Outline each Plasmodium ovale-infected red blood cell.
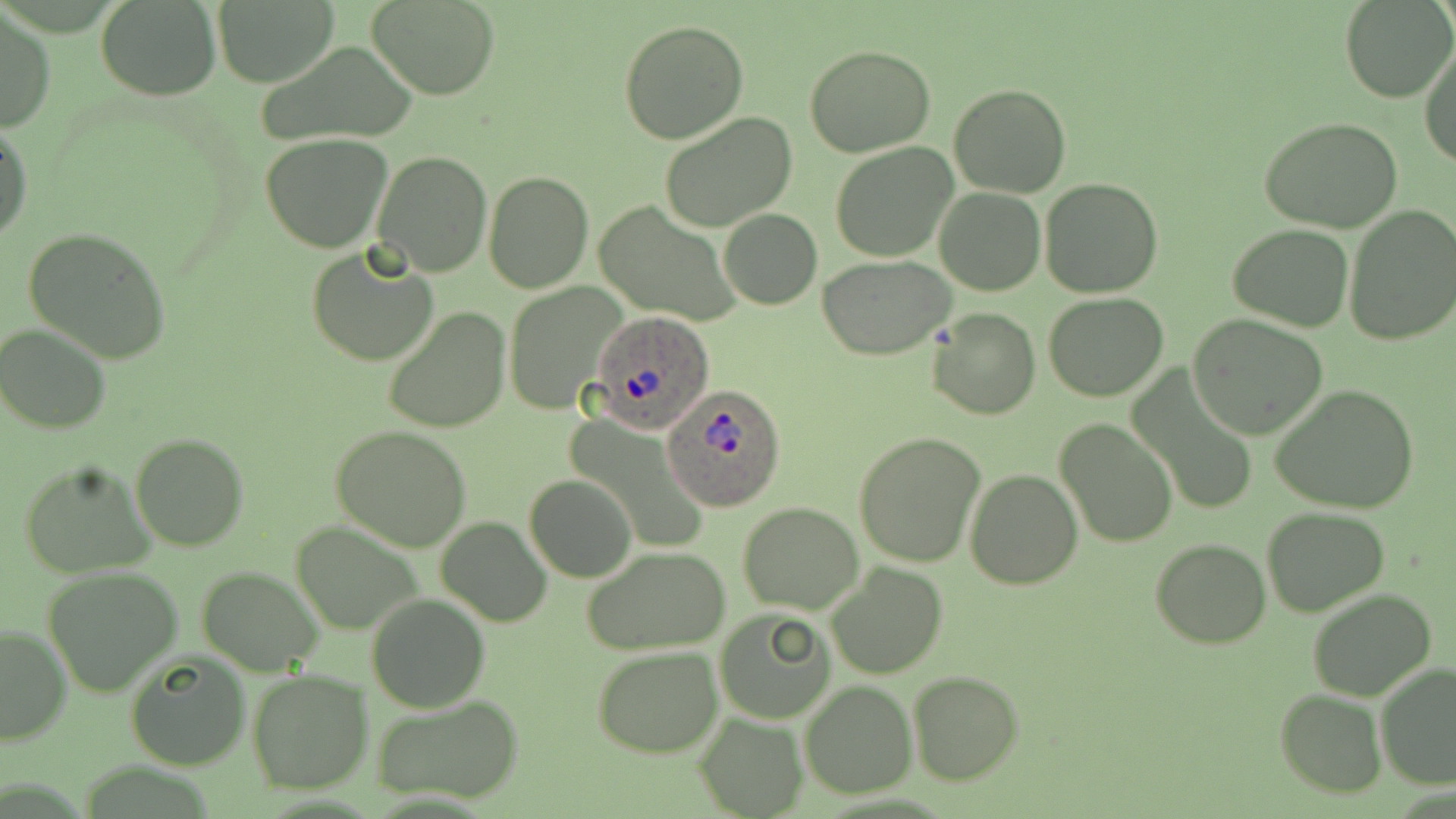

Approximate bounding boxes as (x1, y1, x2, y2) in pixels.
Plasmodium ovale-infected red blood cells: (587, 311, 719, 438), (667, 385, 788, 510).

Summary:
  - Uninfected red blood cell locations: (367, 0, 499, 99), (1340, 0, 1454, 103), (97, 1, 219, 100), (211, 2, 334, 83), (1, 8, 54, 134), (618, 19, 749, 144), (254, 39, 420, 150), (1419, 43, 1456, 167), (804, 44, 937, 157), (949, 84, 1072, 199), (659, 111, 798, 232), (1259, 116, 1404, 233), (0, 118, 33, 245), (261, 134, 394, 252), (831, 142, 960, 262), (370, 151, 493, 278), (482, 171, 595, 294), (1040, 177, 1163, 298), (934, 187, 1045, 296), (594, 199, 740, 326), (1343, 204, 1456, 344), (719, 210, 821, 310), (1228, 223, 1356, 331), (22, 227, 171, 364), (305, 245, 439, 369), (820, 255, 956, 359), (506, 283, 627, 415), (1044, 291, 1168, 401), (382, 306, 512, 433), (927, 307, 1040, 420), (1189, 313, 1329, 440), (1, 324, 113, 433), (1127, 366, 1261, 521), (1269, 384, 1420, 514), (1054, 418, 1179, 549), (330, 424, 476, 554), (855, 430, 985, 568), (130, 431, 249, 552), (17, 458, 155, 579), (964, 468, 1083, 589), (525, 474, 636, 583), (737, 502, 864, 614), (1263, 506, 1390, 618), (436, 515, 552, 626), (289, 520, 427, 636), (1151, 538, 1272, 649), (582, 544, 731, 655), (826, 563, 947, 679), (197, 565, 323, 676), (43, 566, 184, 696), (1307, 587, 1436, 701), (365, 594, 490, 713), (715, 609, 837, 724), (0, 625, 71, 745), (591, 644, 725, 759), (125, 652, 251, 771), (1373, 662, 1456, 789), (247, 669, 374, 794), (908, 672, 1025, 786), (799, 681, 916, 799), (1275, 689, 1388, 798), (373, 695, 524, 806), (695, 710, 808, 817)
  - Slide-level diagnosis: Plasmodium ovale
  - Magnification: 1000x
  - Image size: 1456×819 pixels
  - Modality: light microscopy
  - Stain: May-Grünwald-Giemsa
  - Preparation: thin blood smear
  - Field of view: one of a larger specimen